Comment on the morphology of the red blood cells.
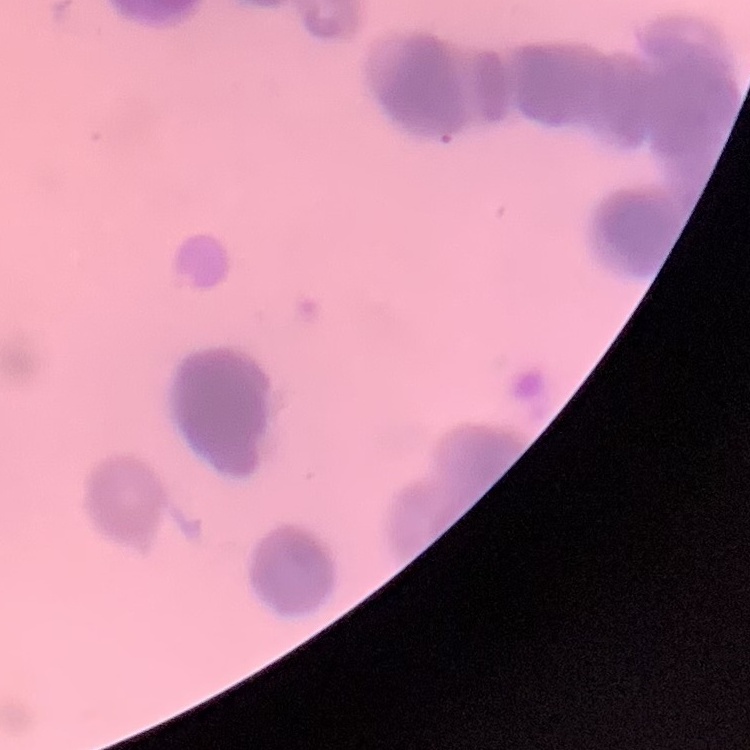

Rouleaux formation.

Summary:
  - Preparation: thin blood film
  - Image type: one tile cut from a larger photomicrograph
  - Stain: Field's or Giemsa